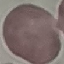
malaria_status: uninfected
stain: Giemsa
preparation: thin blood film
capture: smartphone through the microscope eyepiece
image_type: cell patch, automatically extracted from a larger field of view and resized to 64 × 64 pixels